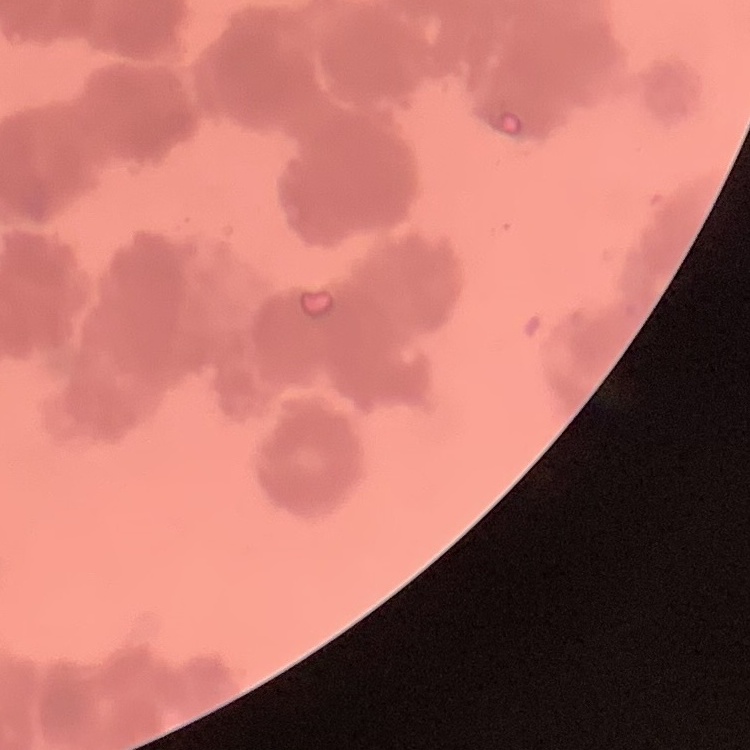

The erythrocytes exhibit rouleaux formation. Field's or Giemsa stain. Thin peripheral smear. Square crop of a larger photomicrograph.